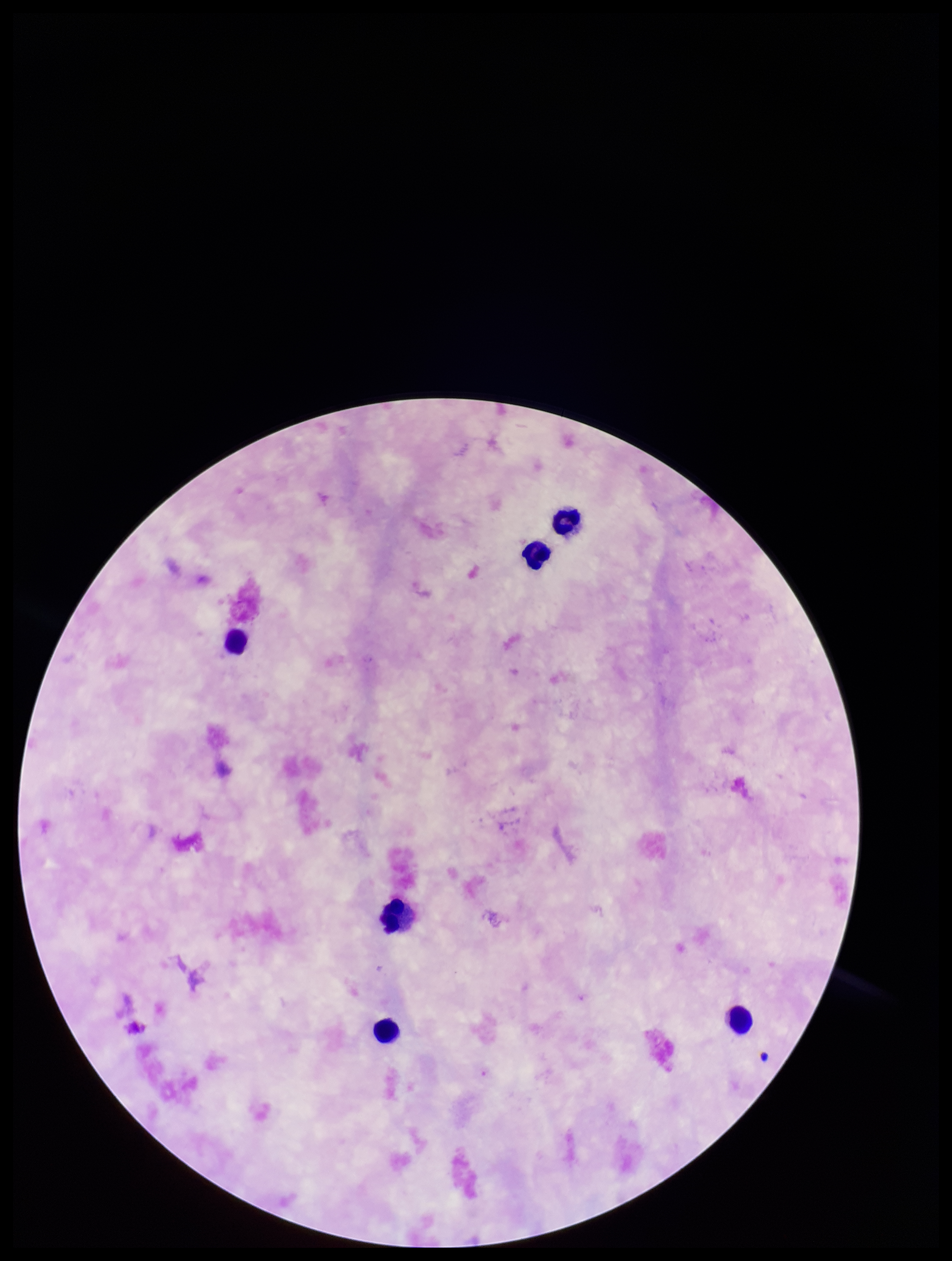
patient malaria status = negative
leukocyte count = 6
capture = smartphone photograph through the microscope eyepiece
field of view = one from this slide
stain = Giemsa
preparation = thick
image size = 952×1261 pixels
Plasmodium parasites = none detected
parasite count = 0